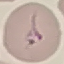 Malaria status: uninfected. Cell patch, automatically extracted from a larger field of view and resized to 64 × 64 pixels. Giemsa-stained preparation. Thin blood film. Photographed with a smartphone camera at the microscope eyepiece.